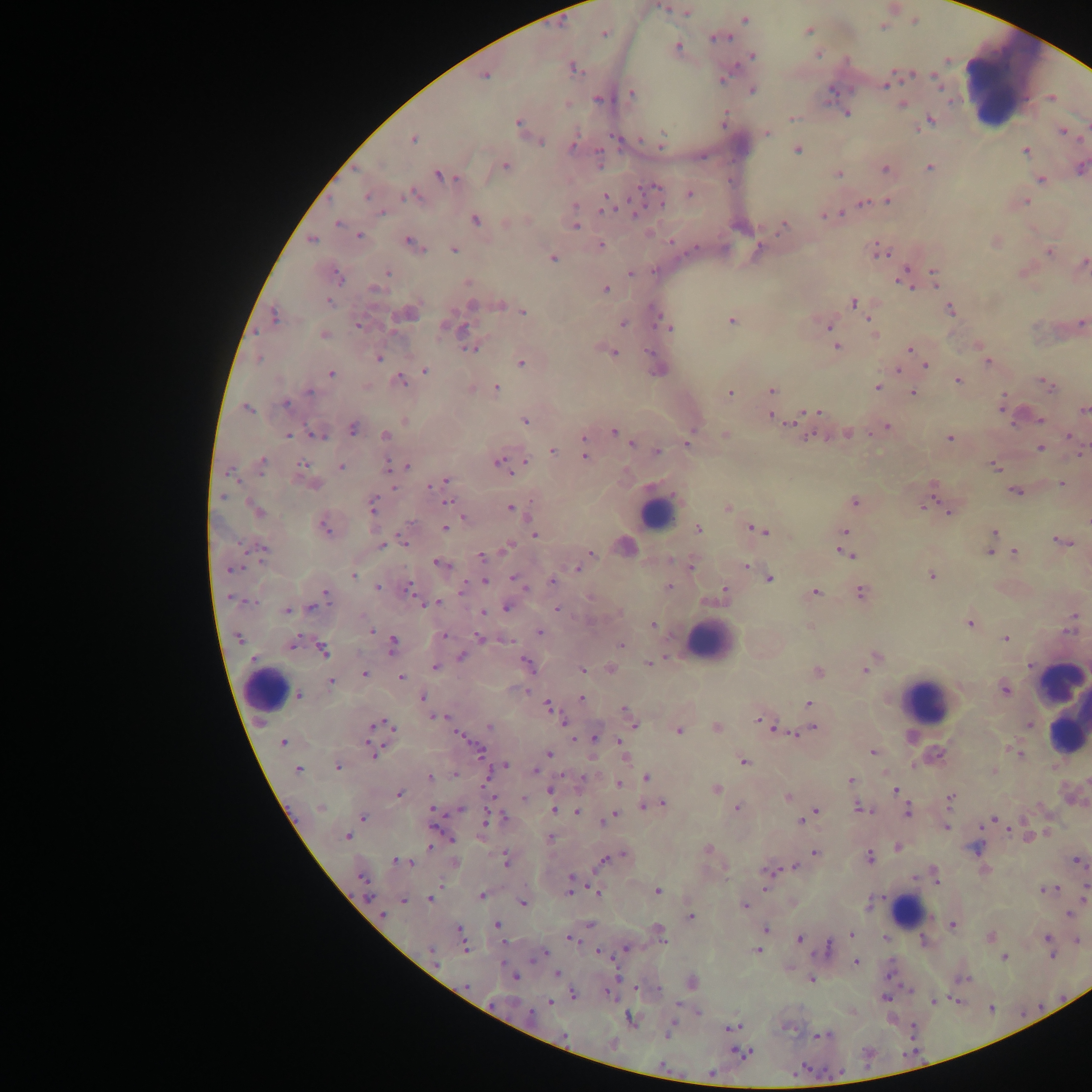
Approximate centers as [x, y] in pixels.
Summary:
  - Leukocyte locations: [1012, 87], [654, 511], [706, 642], [266, 689], [928, 703], [1068, 707], [907, 912]
  - Plasmodium parasite locations: [664, 8], [744, 18], [914, 22], [885, 27], [809, 31], [604, 35], [731, 37], [712, 39], [677, 45], [818, 54], [753, 55], [951, 60], [913, 75], [723, 79], [886, 87], [942, 87], [753, 91], [631, 92], [962, 98], [596, 99], [954, 101], [826, 105], [901, 105], [848, 113], [931, 118], [791, 119], [517, 123], [1060, 128], [664, 131], [767, 133], [612, 136], [575, 137], [413, 139], [640, 139], [662, 140], [542, 142], [574, 144], [661, 146], [797, 149], [1026, 151], [597, 153], [703, 158], [506, 167], [599, 167], [931, 167], [884, 170], [438, 174], [839, 174], [656, 186], [412, 191], [690, 194], [367, 195], [405, 196], [605, 197], [626, 199], [887, 200], [1027, 202], [663, 204], [861, 204], [381, 212], [841, 212], [601, 213], [635, 214], [823, 216], [476, 220], [338, 222], [506, 223], [576, 227], [776, 234], [358, 235], [313, 240], [407, 240], [671, 241], [602, 244], [875, 244], [695, 249], [425, 250], [454, 250], [1048, 252], [887, 257], [553, 258], [1083, 262], [906, 267], [336, 269], [653, 271], [932, 271], [387, 272], [630, 273], [899, 281], [935, 285], [606, 289], [911, 289], [329, 301], [853, 303], [950, 309], [522, 311], [273, 315], [658, 315], [868, 318], [654, 320], [731, 320], [621, 323], [1082, 323], [359, 325], [828, 326], [672, 329], [464, 330], [323, 333], [467, 338], [470, 347], [837, 347], [908, 350], [615, 352], [259, 359], [379, 359], [987, 361], [522, 363], [925, 365], [897, 370], [426, 371], [331, 373], [399, 377], [958, 380], [402, 382], [405, 385], [496, 387], [1050, 387], [877, 388], [771, 389], [730, 391], [308, 392], [913, 392], [1003, 395], [286, 404], [247, 409], [819, 411], [1084, 411], [770, 416], [1041, 419], [525, 420], [788, 424], [1012, 424], [888, 427], [351, 429], [614, 432], [310, 434], [813, 434], [289, 435], [871, 435], [1067, 435], [385, 436], [584, 439], [949, 439], [633, 444], [686, 445], [1040, 447], [552, 450], [656, 451], [1082, 452], [584, 456], [263, 460], [498, 460], [525, 461], [302, 463], [387, 466], [406, 466], [995, 467], [342, 468], [510, 473], [263, 474], [234, 480], [238, 480], [445, 480], [1059, 483], [933, 486], [429, 487], [393, 488], [1015, 491], [375, 496], [219, 497], [448, 501], [854, 501], [248, 502], [374, 502], [928, 502], [510, 508], [372, 512], [947, 512], [259, 513], [324, 527], [444, 528], [749, 528], [845, 531], [766, 532], [994, 532], [535, 536], [1055, 540], [404, 542], [1067, 542], [510, 544], [383, 545], [505, 547], [262, 548], [837, 548], [254, 550], [247, 551], [991, 552], [1014, 552], [591, 553], [1004, 553], [480, 556], [853, 556], [435, 562], [262, 563], [746, 566], [576, 568], [228, 571], [932, 575], [353, 576], [512, 576], [769, 579], [551, 581], [485, 582], [465, 586], [670, 586], [378, 588], [461, 589], [411, 590], [525, 590], [723, 591], [326, 592], [815, 592], [860, 592], [251, 602], [420, 602], [440, 602], [310, 608], [506, 608], [555, 610], [287, 611], [483, 611], [1073, 616], [970, 623], [1073, 624], [652, 625], [373, 632], [539, 632], [299, 635], [444, 636], [240, 637], [479, 637], [1005, 637], [509, 640], [393, 641], [293, 644], [621, 645], [322, 651], [253, 656], [461, 657], [875, 657], [523, 659], [649, 664], [434, 666], [1029, 666], [582, 670], [866, 670], [363, 674], [401, 676], [330, 680], [1005, 689], [528, 692], [422, 697], [582, 697], [299, 698], [809, 703], [548, 706], [624, 709], [432, 717], [448, 718], [758, 719], [563, 724], [635, 725], [1029, 725], [488, 726], [772, 727], [392, 728], [813, 729], [678, 731], [795, 732], [457, 733], [594, 738], [463, 739], [575, 741], [617, 741], [283, 742], [374, 744], [1006, 748], [480, 749], [872, 753], [550, 754], [1020, 755], [744, 760], [913, 764], [507, 766], [337, 767], [298, 769], [536, 770], [455, 775], [561, 775], [582, 775], [430, 777], [645, 778], [851, 780], [618, 783], [717, 787], [549, 789], [896, 790], [399, 794], [951, 796], [494, 797], [788, 797], [662, 802], [858, 807], [431, 808], [643, 808], [737, 808], [462, 809], [554, 810], [816, 810], [907, 810], [577, 811], [565, 812], [616, 813], [505, 817], [364, 818], [992, 818], [486, 819], [800, 820], [603, 823], [484, 824], [435, 828], [946, 828], [980, 828], [1007, 830], [348, 837], [453, 841], [430, 846], [977, 848], [624, 851], [813, 852], [869, 856], [393, 858], [605, 859], [506, 862], [413, 863], [795, 866], [765, 871], [774, 871], [361, 877], [568, 877], [914, 878], [937, 883], [569, 889], [764, 889], [1040, 890], [1056, 890], [659, 892], [569, 893], [598, 893], [371, 896], [884, 896], [481, 897], [430, 898], [403, 901], [522, 904], [745, 905], [1068, 912], [382, 914], [691, 916], [497, 923], [952, 924], [766, 929], [459, 930], [850, 933], [567, 938], [799, 938], [885, 938], [663, 939], [924, 939], [829, 944], [466, 948], [625, 948], [758, 950], [430, 951], [545, 951], [597, 951], [1005, 957], [854, 958], [1053, 958], [856, 961], [532, 962], [503, 964], [617, 971], [555, 973], [890, 976], [515, 979], [811, 980], [635, 988], [659, 988], [606, 990], [910, 991], [574, 994], [951, 998], [886, 999], [957, 1000], [932, 1002], [550, 1003], [1042, 1006], [991, 1009], [673, 1023], [727, 1027], [739, 1027], [911, 1029], [819, 1034], [814, 1035], [734, 1048], [748, 1052], [911, 1053], [666, 1069], [803, 1069], [843, 1069], [710, 1073]
  - Image size: 1092×1092 pixels
  - Field of view: single
  - Capture: mobile-phone photograph through a microscope
  - Preparation: thick blood smear
  - Country: Ghana